Classify this cell by malaria status.
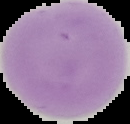

It is uninfected.

{
  "preparation": "thin blood smear",
  "image_type": "segmented cell region on a black background",
  "image_size": "130×124 pixels"
}